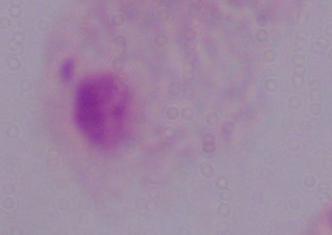
magnification = 1000x
modality = photomicrograph
identification = trichomonad